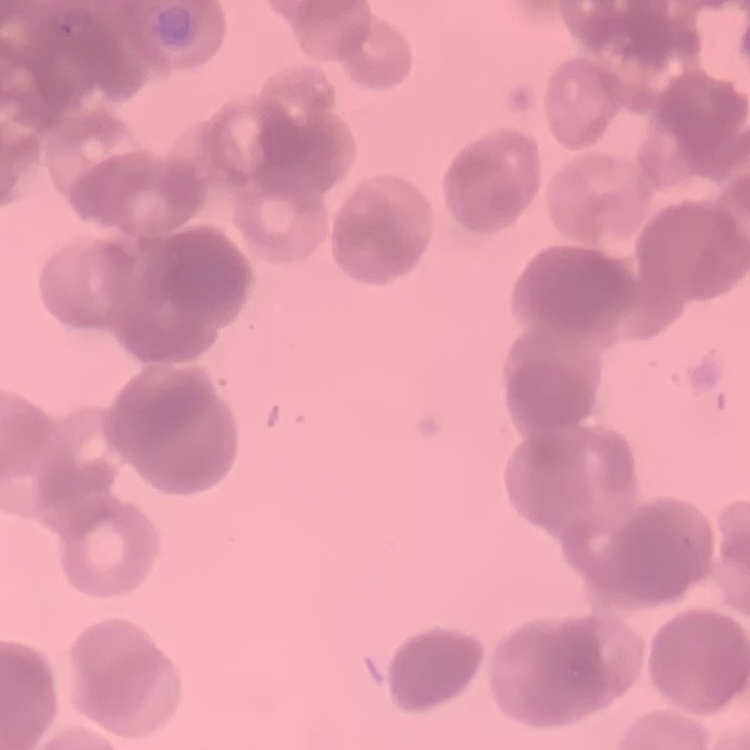
Summary:
  - Red blood cell morphology: rouleaux formation
  - Preparation: thin peripheral smear
  - Image type: one tile cut from a larger photomicrograph
  - Stain: Field's or Giemsa